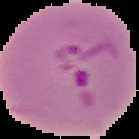 Image is 139×139 pixels. Result: malaria parasites detected. The area outside the segmented cell region is set to black. From a thin blood smear.